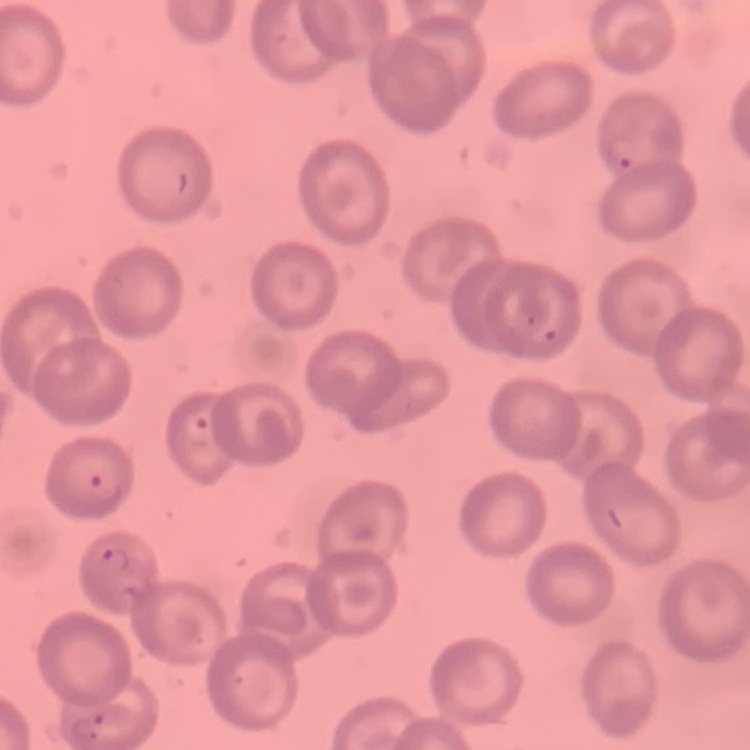

The red blood cells show no rouleaux formation. One tile cut from a larger photomicrograph. Stained with either Field's or Giemsa. Thin blood smear.